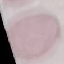
malaria_status: uninfected
capture: smartphone camera at the microscope eyepiece
image_type: cell patch, automatically extracted from a larger field of view and resized to 64 × 64 pixels
preparation: thin smear
stain: Giemsa